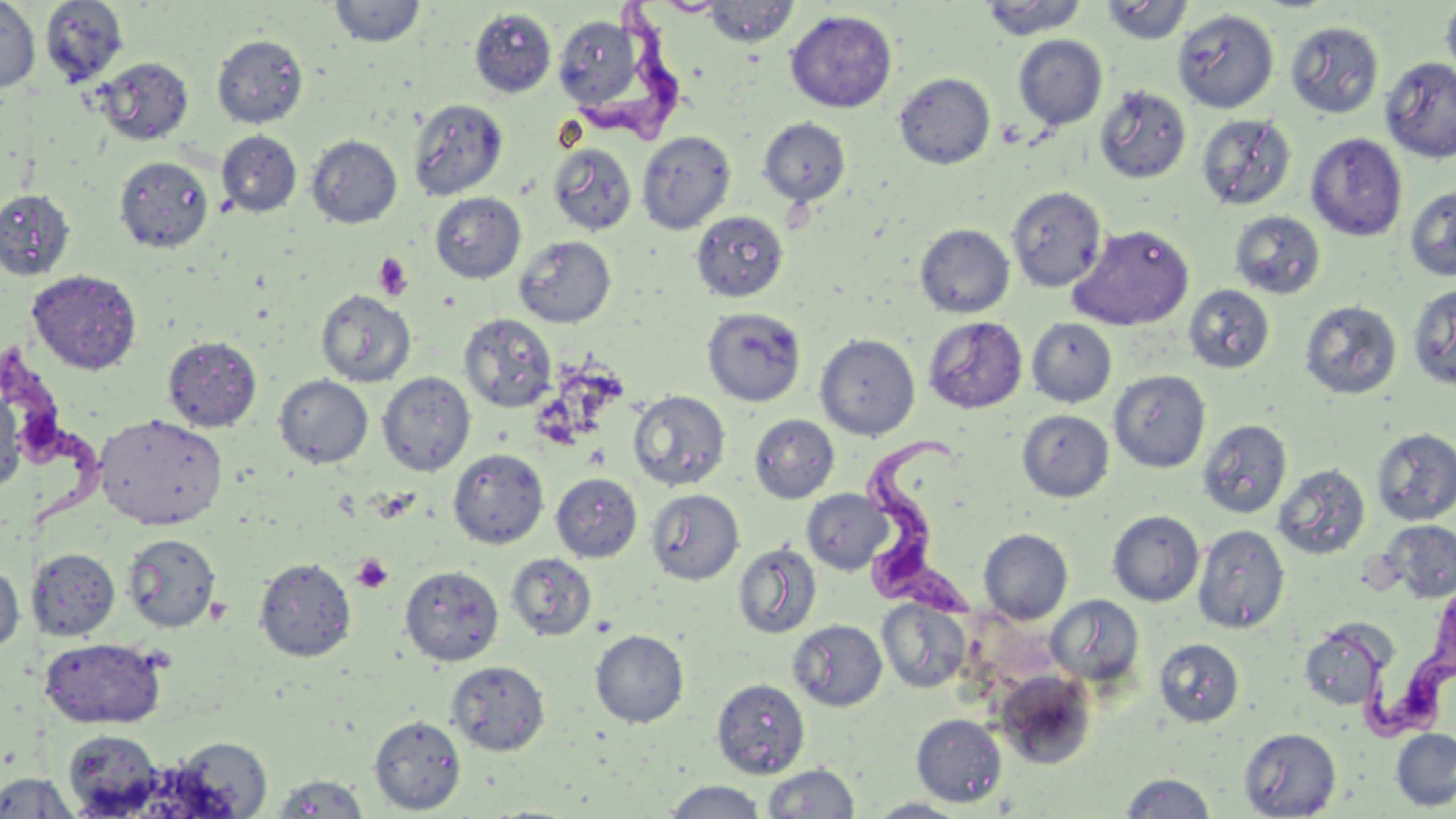

Approximate bounding boxes as (x1, y1, x2, y2) in pixels. Trypanosoma brucei locations: (583, 0, 697, 149), (0, 334, 98, 530), (861, 435, 975, 615), (1318, 600, 1456, 747). Uninfected red blood cell locations: (40, 0, 128, 87), (979, 0, 1090, 40), (1100, 0, 1193, 46), (1441, 0, 1456, 85), (0, 1, 40, 92), (329, 1, 425, 48), (654, 1, 727, 16), (702, 1, 800, 47), (469, 8, 557, 98), (1173, 8, 1279, 112), (785, 10, 898, 112), (553, 15, 647, 112), (1285, 21, 1384, 119), (212, 34, 308, 128), (1013, 35, 1108, 129), (93, 56, 194, 146), (1380, 56, 1456, 163), (894, 72, 995, 169), (1094, 85, 1192, 184), (408, 98, 508, 200), (1196, 113, 1296, 211), (758, 117, 851, 207), (216, 130, 302, 217), (636, 131, 736, 234), (1306, 133, 1407, 242), (306, 135, 402, 228), (548, 143, 638, 236), (114, 155, 214, 253), (1006, 185, 1106, 292), (1405, 185, 1456, 282), (0, 188, 76, 281), (430, 192, 526, 283), (690, 209, 789, 302), (1229, 210, 1326, 299), (915, 224, 1015, 317), (1068, 224, 1195, 331), (513, 235, 616, 328), (27, 269, 142, 375), (1407, 282, 1456, 390), (1184, 285, 1275, 374), (315, 289, 416, 387), (1300, 300, 1402, 399), (701, 307, 806, 406), (459, 312, 557, 412), (923, 315, 1028, 413), (1027, 317, 1117, 407), (815, 332, 921, 441), (163, 335, 262, 431), (1109, 370, 1210, 472), (377, 372, 476, 476), (274, 375, 373, 468), (0, 381, 24, 495), (628, 390, 731, 490), (1017, 410, 1114, 502), (95, 412, 227, 530), (749, 414, 839, 503), (1198, 418, 1292, 519), (1372, 427, 1456, 525), (448, 449, 549, 549), (1273, 463, 1371, 560), (551, 473, 642, 562), (646, 488, 744, 585), (802, 489, 893, 575), (1107, 510, 1204, 606), (1382, 519, 1456, 603), (1192, 523, 1290, 633), (979, 528, 1073, 623), (122, 533, 222, 632), (733, 542, 822, 639), (27, 549, 120, 640), (505, 552, 597, 641), (253, 557, 356, 661), (0, 563, 25, 653), (400, 564, 504, 666), (1046, 595, 1145, 689), (878, 599, 971, 693), (788, 619, 887, 711), (1298, 622, 1391, 710), (590, 629, 689, 727), (39, 637, 166, 729), (1153, 639, 1244, 726), (446, 660, 550, 755), (995, 671, 1099, 768), (711, 677, 810, 778), (911, 714, 1007, 806), (369, 715, 466, 814), (1238, 727, 1341, 817), (1391, 728, 1456, 811), (62, 729, 165, 816), (166, 736, 273, 817), (762, 763, 860, 819), (0, 771, 79, 818), (1118, 772, 1218, 818), (270, 773, 372, 818), (662, 780, 769, 818), (865, 797, 972, 818). Platelet locations: (373, 253, 414, 301), (351, 553, 394, 593). Slide-level diagnosis: Trypanosoma brucei. Image is 1456×819 pixels. Optical microscopy. Single field of view. Thin blood film. 1000x magnification. May-Grünwald-Giemsa stain.